Name the blood parasite species.
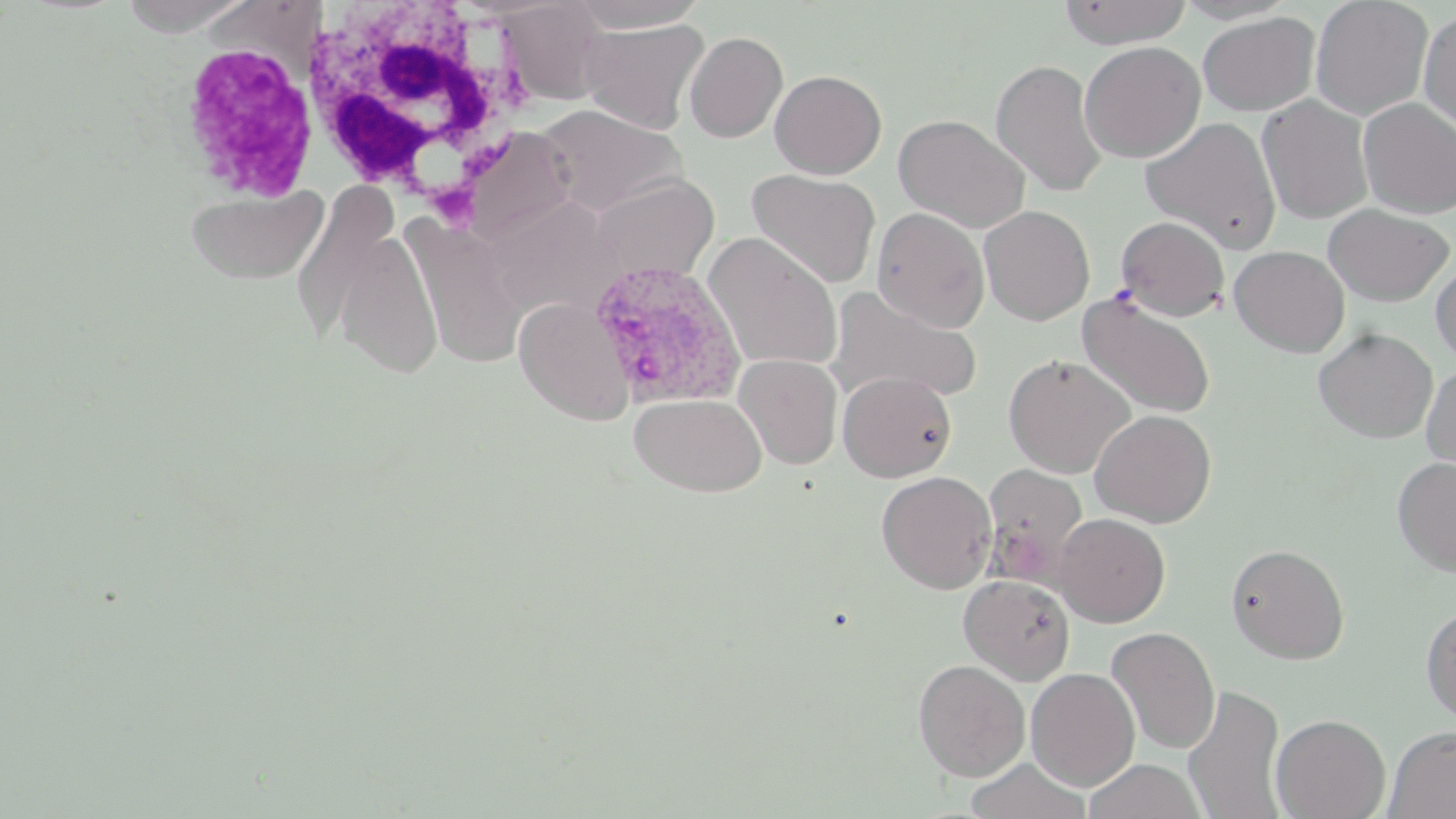
Plasmodium ovale.

{
  "modality": "light microscopy",
  "magnification": "1000x",
  "preparation": "thin blood film",
  "stain": "May-Grünwald-Giemsa",
  "white_blood_cell_locations": "approximate bounding boxes as (x1, y1, x2, y2) in pixels: (300, 1, 537, 204), (175, 39, 319, 204)",
  "field_of_view": "one of a larger specimen",
  "uninfected_red_blood_cell_locations": "approximate bounding boxes as (x1, y1, x2, y2) in pixels: (114, 0, 257, 35), (562, 0, 712, 31), (1058, 0, 1191, 48), (1171, 0, 1300, 24), (1310, 0, 1433, 120), (496, 2, 611, 104), (1418, 9, 1456, 136), (1197, 11, 1320, 116), (578, 19, 710, 134), (684, 31, 788, 143), (1078, 41, 1205, 162), (991, 58, 1107, 197), (770, 70, 886, 178), (1257, 95, 1374, 224), (1357, 99, 1456, 218), (533, 105, 688, 216), (894, 113, 1030, 233), (1140, 116, 1281, 253), (457, 124, 580, 244), (746, 169, 881, 289), (588, 175, 719, 284), (289, 183, 400, 350), (186, 186, 329, 285), (1323, 204, 1454, 306), (979, 205, 1095, 325), (872, 208, 990, 332), (1115, 216, 1230, 320), (407, 221, 529, 368), (335, 228, 444, 379), (704, 232, 843, 373), (1229, 245, 1349, 357), (1431, 261, 1456, 366), (827, 286, 983, 404), (1076, 293, 1216, 418), (514, 297, 634, 425), (1314, 327, 1438, 443), (1002, 353, 1135, 478), (734, 354, 843, 469), (1421, 362, 1456, 480), (838, 372, 956, 482), (630, 393, 766, 497), (1090, 409, 1216, 527), (1392, 455, 1456, 577), (981, 463, 1088, 588), (876, 471, 997, 593), (1053, 512, 1170, 627), (1225, 543, 1349, 663), (959, 575, 1076, 685), (1421, 605, 1456, 725), (1106, 626, 1220, 755), (912, 659, 1030, 781), (1025, 667, 1140, 791), (1183, 684, 1287, 819), (1271, 713, 1391, 819), (1384, 726, 1456, 818), (965, 759, 1091, 819), (1085, 759, 1206, 819)",
  "image_size": "1456×819 pixels",
  "plasmodium_ovale_infected_red_blood_cell_locations": "approximate bounding boxes as (x1, y1, x2, y2) in pixels: (584, 258, 747, 408)"
}